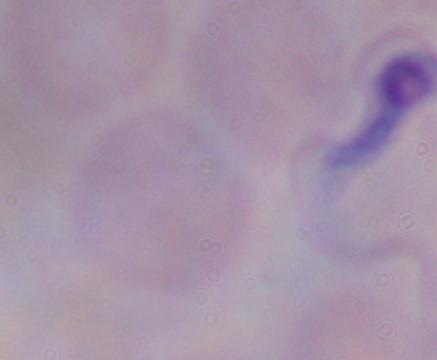

Summary:
  - Identification: trypanosome
  - Modality: micrograph
  - Magnification: 1000x